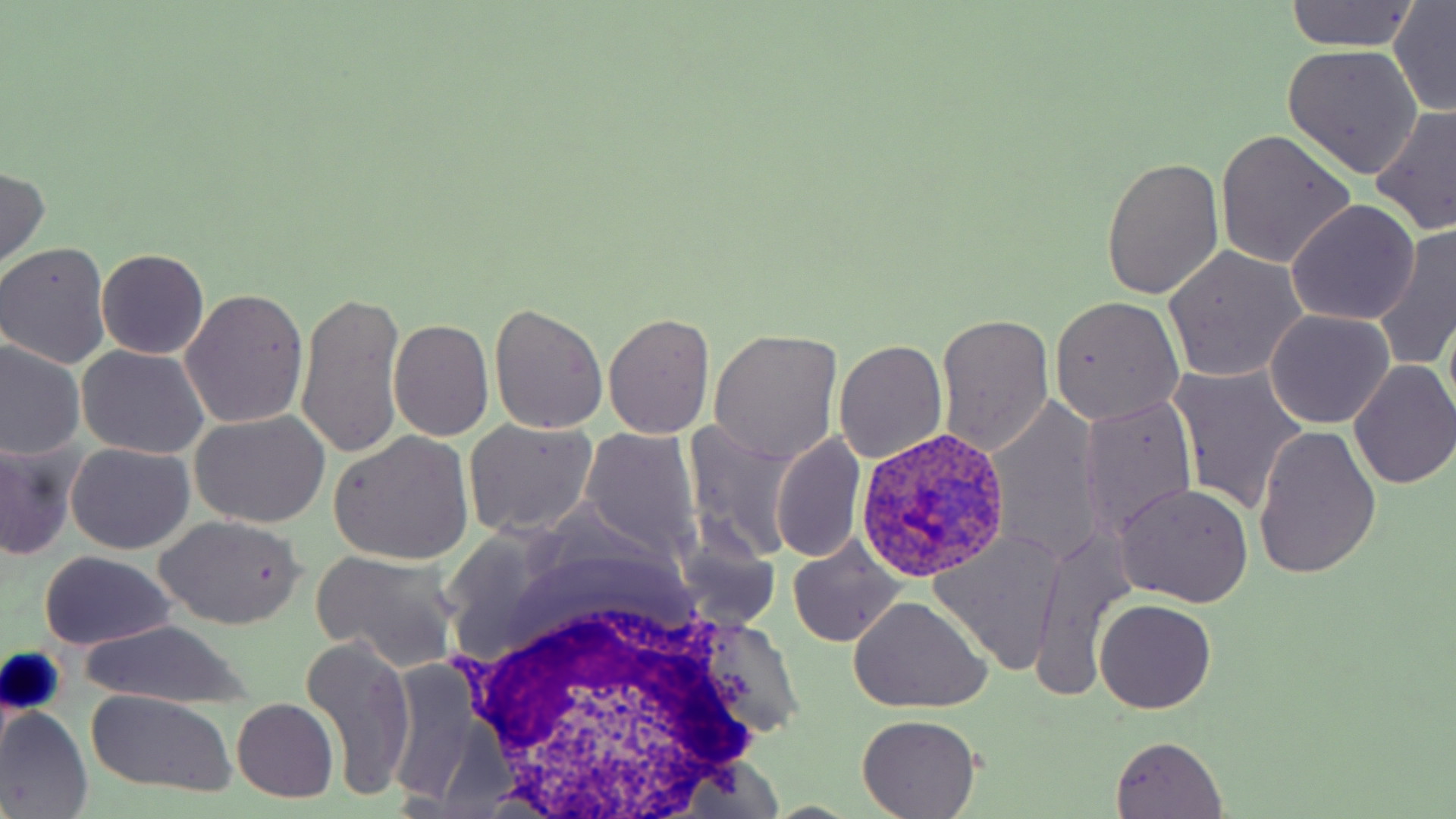

Approximate bounding boxes as (x1, y1, x2, y2) in pixels. White blood cell locations: (441, 559, 785, 812). Plasmodium ovale-infected red blood cell locations: (852, 428, 1017, 582). Uninfected red blood cell locations: (1283, 1, 1421, 53), (1387, 1, 1456, 115), (1283, 45, 1423, 178), (1370, 103, 1456, 237), (1215, 132, 1355, 268), (1101, 156, 1225, 299), (0, 165, 50, 272), (1285, 201, 1419, 326), (1373, 223, 1456, 371), (0, 242, 112, 370), (1164, 245, 1309, 382), (98, 250, 208, 360), (179, 288, 311, 430), (297, 288, 407, 461), (1047, 295, 1185, 426), (489, 302, 608, 435), (1264, 309, 1395, 428), (602, 311, 715, 440), (934, 314, 1056, 456), (389, 319, 494, 441), (707, 330, 842, 463), (834, 339, 947, 465), (0, 340, 86, 462), (76, 345, 211, 460), (1349, 360, 1456, 490), (1170, 365, 1308, 515), (1081, 397, 1198, 545), (987, 399, 1102, 568), (190, 411, 331, 529), (462, 418, 599, 540), (683, 422, 801, 564), (1253, 425, 1381, 581), (578, 428, 702, 562), (328, 431, 475, 565), (770, 432, 865, 564), (0, 438, 78, 564), (67, 443, 195, 555), (1113, 483, 1253, 607), (154, 515, 304, 629), (929, 531, 1067, 673), (671, 532, 781, 634), (1033, 534, 1129, 700), (787, 537, 905, 647), (312, 550, 463, 674), (38, 552, 177, 651), (847, 597, 992, 713), (1094, 598, 1217, 713), (79, 622, 251, 707), (300, 634, 418, 800), (85, 691, 237, 798), (231, 698, 340, 804), (0, 706, 93, 819), (856, 716, 981, 818), (1109, 735, 1229, 818). Slide-level diagnosis: Plasmodium ovale. Single field of view. May-Grünwald-Giemsa-stained preparation. Image is 1456×819 pixels. Thin blood film. Captured at 1000x magnification. Optical microscopy.